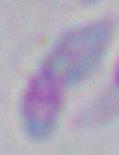

Summary:
  - Modality: micrograph
  - Magnification: 1000x
  - Identification: Toxoplasma gondii